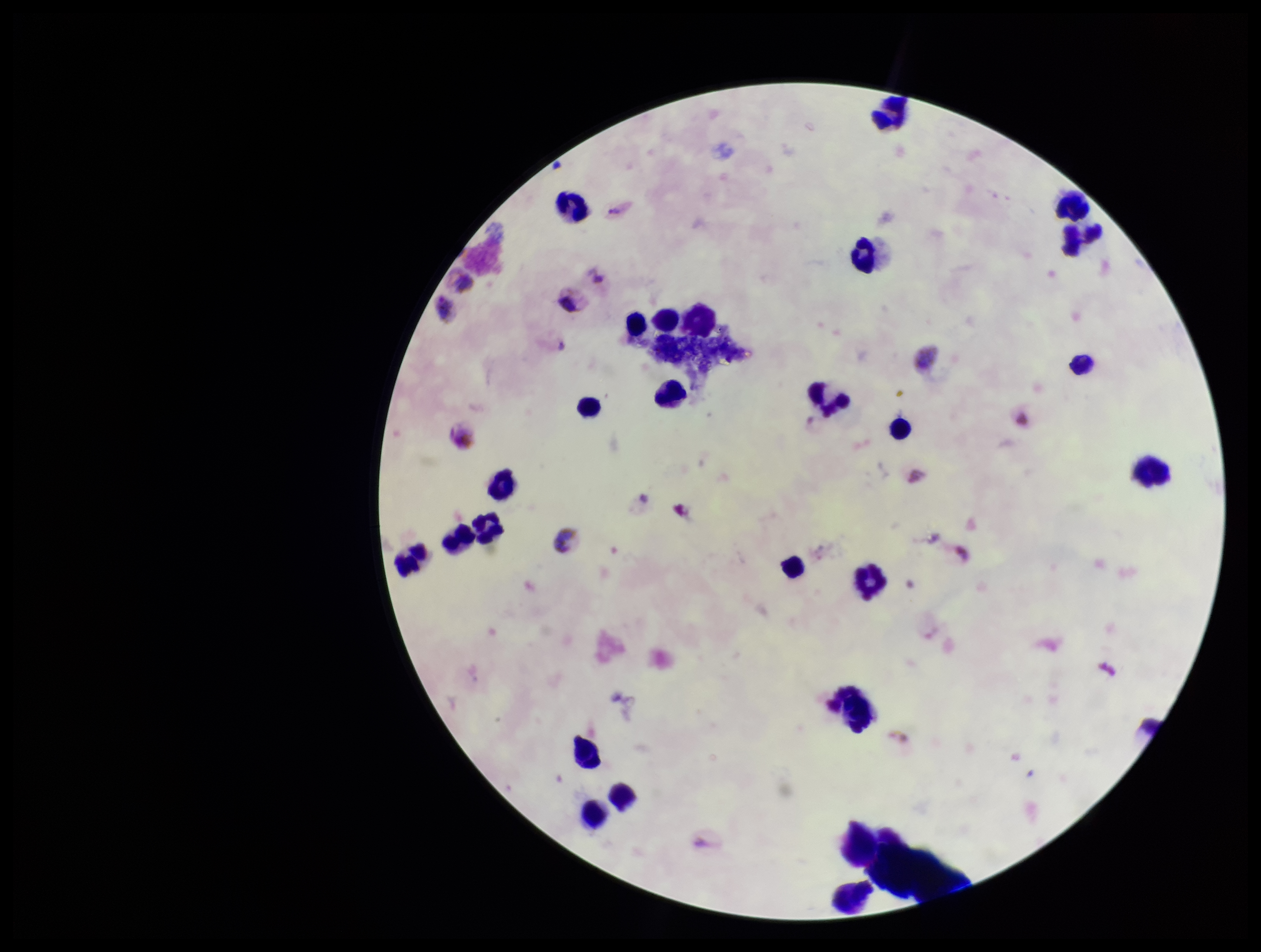

Plasmodium parasites = none identified
field of view = single
stain = Giemsa
preparation = thick smear
capture = smartphone photograph through the microscope eyepiece
species reported for this patient = Plasmodium vivax
leukocyte count = 26
image size = 1261×952 pixels
parasite count = 0
patient malaria status = infected